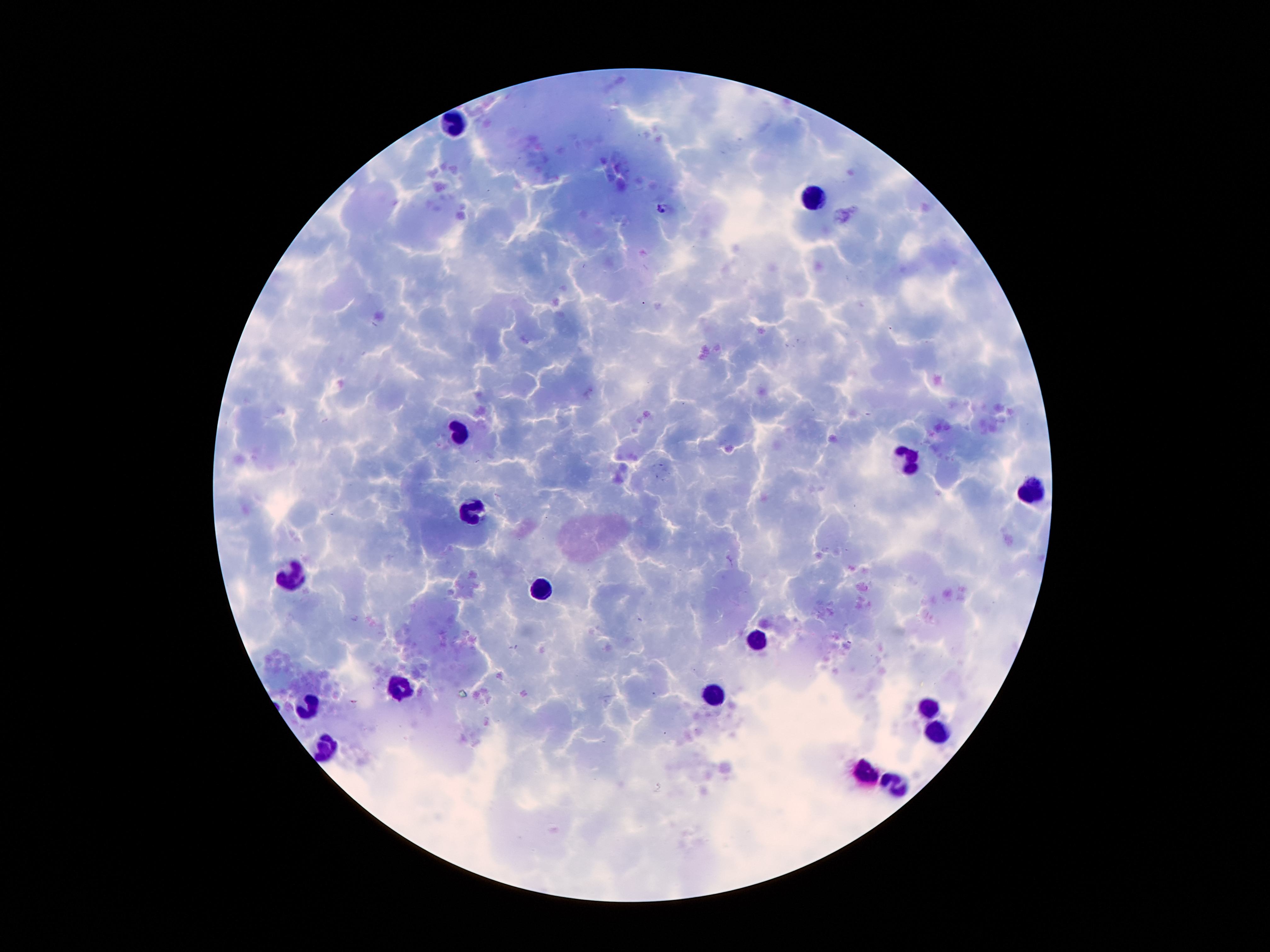

Approximate centers as {x, y} in pixels. Leukocyte locations: {456, 123}, {817, 200}, {458, 434}, {908, 462}, {1035, 491}, {472, 509}, {292, 577}, {540, 591}, {755, 636}, {399, 688}, {717, 693}, {310, 704}, {930, 707}, {939, 736}, {326, 747}, {869, 775}, {899, 782}. Malaria parasite locations: {663, 208}. 100x magnification. Giemsa stain. Single field of view. Patient malaria status: infected with Plasmodium falciparum. Smartphone photograph taken through the microscope eyepiece. Image is 1270×952 pixels. Thick blood film.